Comment on the morphology of the red blood cells.
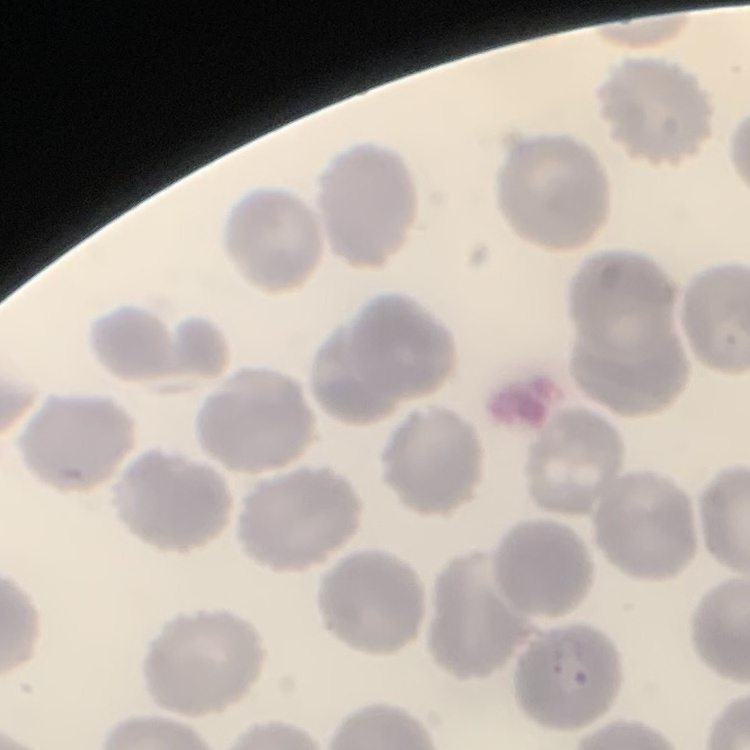

They show no rouleaux formation.

Summary:
  - Preparation: thin blood smear
  - Stain: Field's or Giemsa
  - Image type: one tile cut from a larger photomicrograph